Point out each malaria parasite.
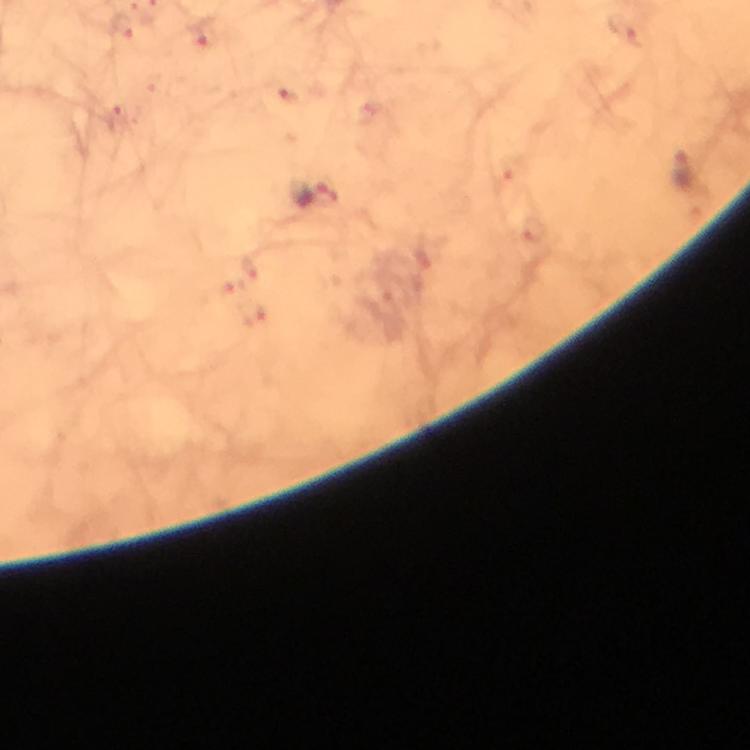

Approximate centers as [x, y] in pixels.
Malaria parasites: [317, 195].

Smartphone photograph taken through a microscope. From a diagnostic examination for malaria. Thick smear. Image is 750×750 pixels. At 100x magnification. Giemsa stain. Immersion oil applied. A crop from one field of view.